Report the malaria status of this cell.
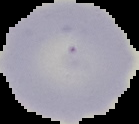

Uninfected.

preparation = thin blood film
image type = segmented cell region on a black background
image size = 139×124 pixels